Name the parasite shown.
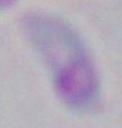
Toxoplasma gondii.

Summary:
  - Modality: micrograph
  - Magnification: 1000x